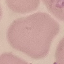

{
  "result": "negative for malaria parasites",
  "preparation": "thin blood smear",
  "capture": "smartphone camera at the microscope eyepiece",
  "image_type": "automatically extracted cell patch, resized to 64 × 64 pixels",
  "stain": "Giemsa"
}